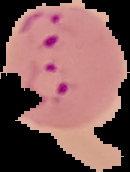
Image is 130×172 pixels. Malaria status: parasitized. Cell region segmented out of the field of view; the surrounding area is masked to black. From a thin blood smear.